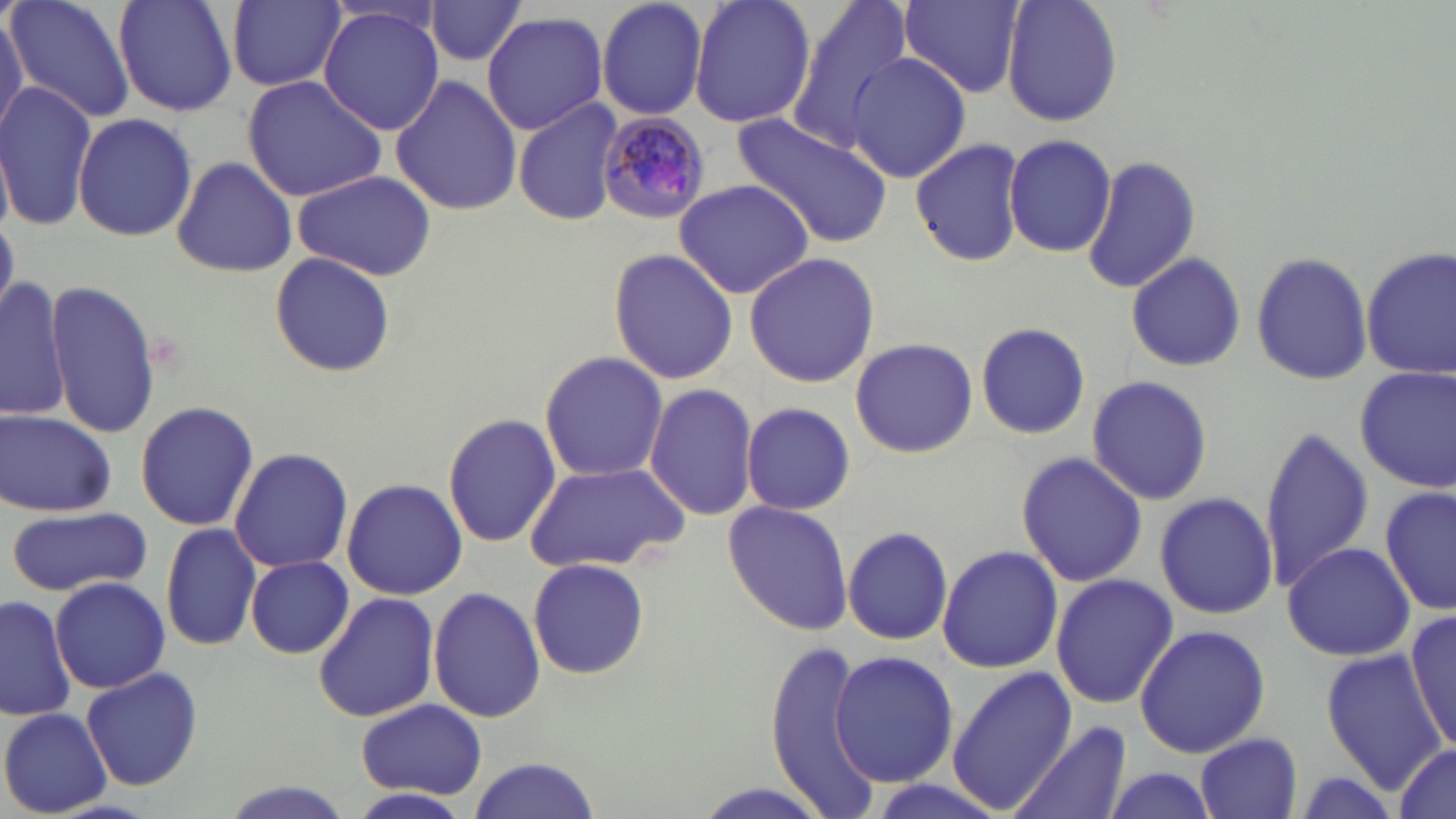

Approximate bounding boxes as (x1, y1, x2, y2) in pixels. Uninfected red blood cell locations: (6, 0, 138, 124), (114, 0, 238, 117), (596, 0, 710, 122), (690, 0, 816, 131), (785, 0, 915, 151), (1000, 0, 1121, 126), (224, 1, 347, 92), (900, 1, 1024, 99), (426, 2, 526, 66), (317, 5, 445, 137), (0, 7, 27, 140), (482, 10, 610, 135), (846, 52, 972, 184), (389, 74, 522, 217), (241, 75, 387, 203), (0, 82, 95, 233), (512, 97, 625, 228), (73, 112, 197, 243), (731, 114, 895, 246), (909, 135, 1027, 270), (1004, 136, 1117, 257), (169, 155, 299, 279), (1081, 156, 1203, 293), (290, 170, 439, 281), (671, 179, 814, 299), (609, 245, 738, 385), (1360, 247, 1455, 380), (1251, 249, 1374, 387), (268, 250, 397, 378), (742, 251, 880, 389), (1125, 251, 1246, 373), (1, 277, 74, 422), (42, 279, 161, 438), (975, 322, 1092, 439), (850, 337, 978, 459), (539, 350, 670, 483), (1355, 365, 1456, 494), (1086, 374, 1214, 505), (644, 385, 760, 521), (134, 401, 258, 532), (742, 402, 855, 515), (0, 409, 117, 518), (441, 413, 560, 548), (1258, 424, 1375, 593), (228, 448, 354, 573), (1016, 451, 1145, 588), (524, 462, 690, 574), (342, 478, 468, 600), (1380, 486, 1454, 616), (1154, 491, 1279, 620), (723, 499, 853, 635), (6, 505, 151, 596), (159, 522, 261, 651), (843, 526, 955, 646), (1282, 541, 1417, 662), (937, 544, 1062, 674), (244, 555, 353, 659), (527, 557, 651, 681), (1051, 572, 1177, 709), (49, 575, 173, 694), (427, 586, 544, 724), (312, 592, 442, 723), (0, 595, 78, 722), (1404, 610, 1455, 747), (1134, 624, 1271, 758), (763, 639, 884, 814), (830, 648, 958, 789), (1321, 650, 1445, 790), (946, 665, 1078, 815), (80, 667, 203, 791), (357, 699, 487, 799), (0, 708, 112, 816), (1009, 720, 1133, 819), (1195, 732, 1302, 818), (1388, 743, 1454, 819), (464, 754, 601, 819), (1096, 765, 1223, 819), (217, 783, 353, 819). Plasmodium malariae-infected red blood cell locations: (594, 112, 710, 223). Slide-level diagnosis: Plasmodium malariae. Image is 1456×819 pixels. May-Grünwald-Giemsa stain. Light microscopy. One field of a larger specimen. Captured at 1000x magnification. Thin blood film.